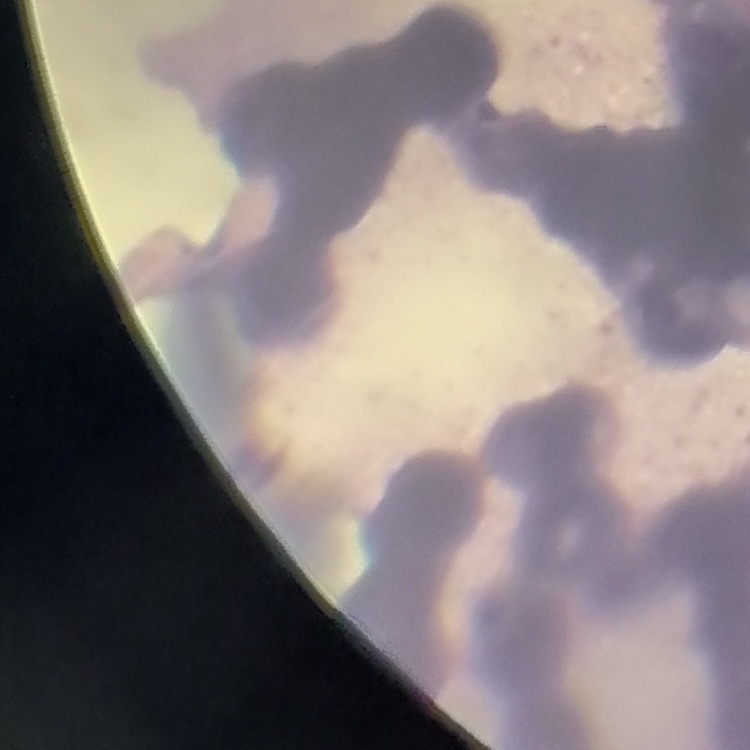

Summary:
  - Erythrocyte morphology: rouleaux formation
  - Preparation: thin blood film
  - Image type: square crop of a larger photomicrograph
  - Stain: Field's or Giemsa